Identify the parasite.
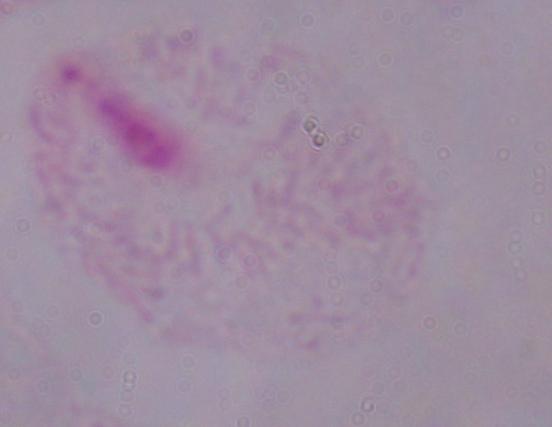

A trichomonad.

{
  "modality": "photomicrograph",
  "magnification": "1000x"
}